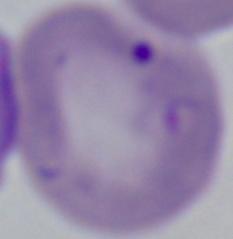 Photomicrograph. Captured at 1000x magnification. A Babesia parasite is seen.